Outline each blood parasite and name the species.
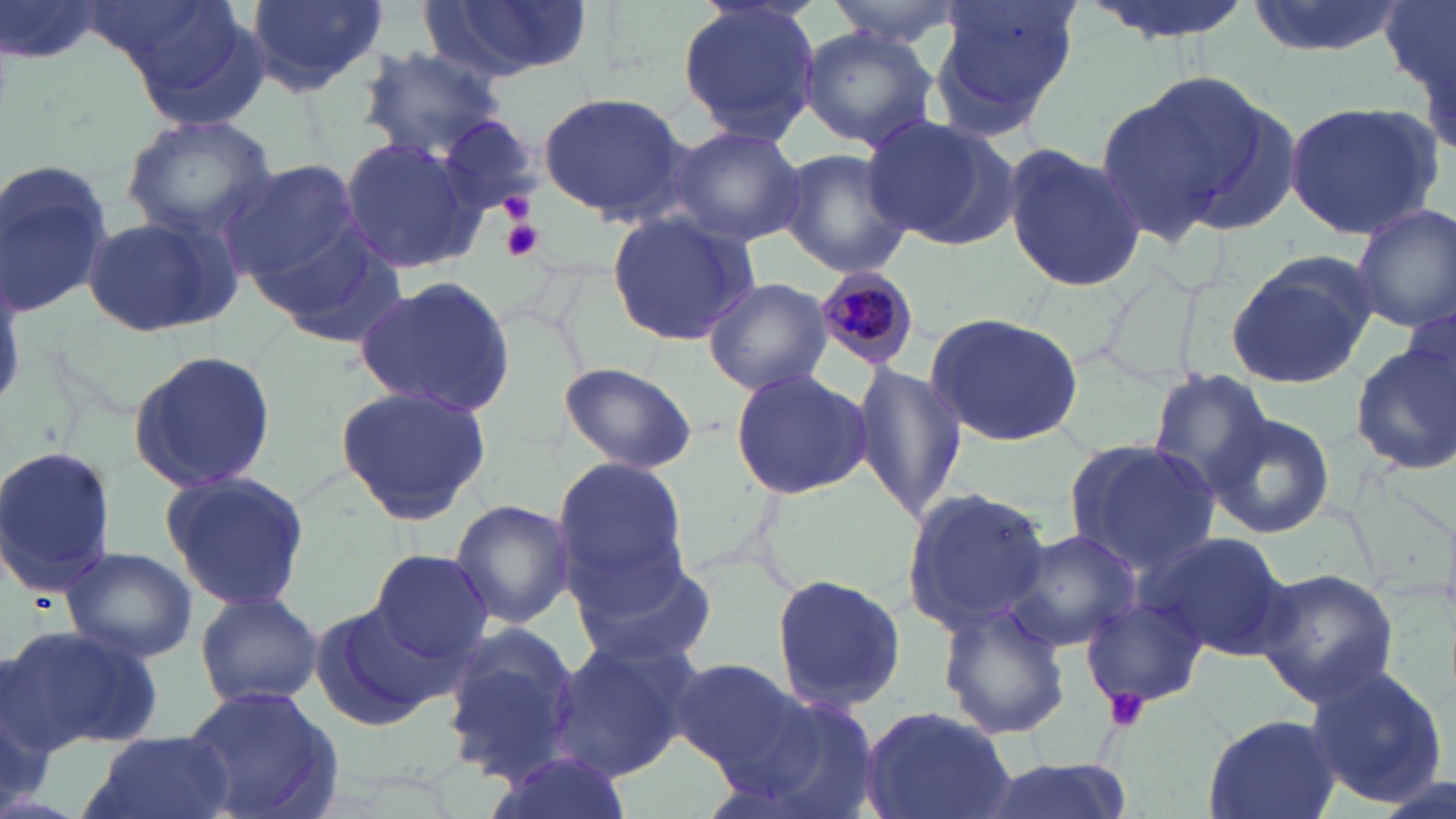
Approximate bounding boxes as (x1, y1, x2, y2) in pixels.
Plasmodium malariae-infected red blood cells: (816, 265, 917, 367).
No Plasmodium falciparum, Plasmodium ovale, Plasmodium vivax, Babesia divergens, or Trypanosoma brucei observed.

Uninfected red blood cell locations: (3, 0, 107, 72), (244, 0, 386, 97), (426, 0, 592, 79), (828, 0, 964, 48), (928, 0, 1080, 134), (1082, 0, 1258, 44), (1242, 0, 1400, 56), (1379, 0, 1455, 100), (679, 1, 820, 145), (99, 2, 274, 129), (798, 25, 938, 150), (356, 46, 509, 160), (1093, 77, 1260, 243), (536, 90, 688, 221), (1284, 101, 1442, 241), (120, 114, 278, 243), (861, 114, 1014, 246), (432, 115, 542, 217), (662, 124, 808, 248), (336, 132, 487, 276), (1003, 144, 1146, 293), (778, 146, 914, 279), (0, 159, 118, 322), (223, 159, 364, 288), (1350, 203, 1455, 333), (605, 209, 759, 348), (82, 212, 238, 340), (259, 226, 408, 351), (1226, 253, 1378, 389), (352, 276, 518, 416), (705, 278, 832, 395), (1399, 300, 1456, 409), (922, 311, 1087, 447), (1353, 342, 1456, 475), (125, 348, 277, 493), (555, 361, 698, 475), (850, 363, 968, 527), (730, 368, 872, 499), (1149, 371, 1275, 497), (334, 383, 491, 526), (1207, 411, 1335, 538), (1063, 439, 1219, 573), (0, 444, 117, 597), (550, 455, 693, 600), (160, 469, 314, 611), (900, 486, 1053, 637), (447, 498, 576, 627), (1140, 529, 1293, 661), (1007, 530, 1140, 653), (570, 544, 717, 671), (62, 547, 197, 662), (369, 549, 495, 666), (1253, 568, 1399, 702), (770, 573, 907, 711), (194, 591, 323, 710), (1080, 592, 1210, 712), (310, 603, 446, 733), (934, 604, 1070, 740), (438, 620, 587, 779), (6, 624, 163, 753), (545, 636, 699, 778), (667, 656, 801, 772), (1305, 661, 1451, 807), (179, 684, 346, 819), (733, 684, 884, 818), (856, 704, 1016, 819), (1203, 712, 1341, 819), (81, 732, 232, 819), (479, 747, 634, 819), (972, 755, 1131, 819), (1377, 771, 1451, 819). Platelet locations: (499, 193, 537, 223), (499, 219, 545, 262), (1104, 687, 1151, 733). Slide-level diagnosis: Plasmodium malariae. Captured at 1000x magnification. Thin blood film. Light microscopy. Single field of view. May-Grünwald-Giemsa stain. Image is 1456×819 pixels.